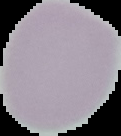

preparation = thin blood film
image size = 121×136 pixels
result = negative for Plasmodium parasites
image type = segmented cell region on a black background